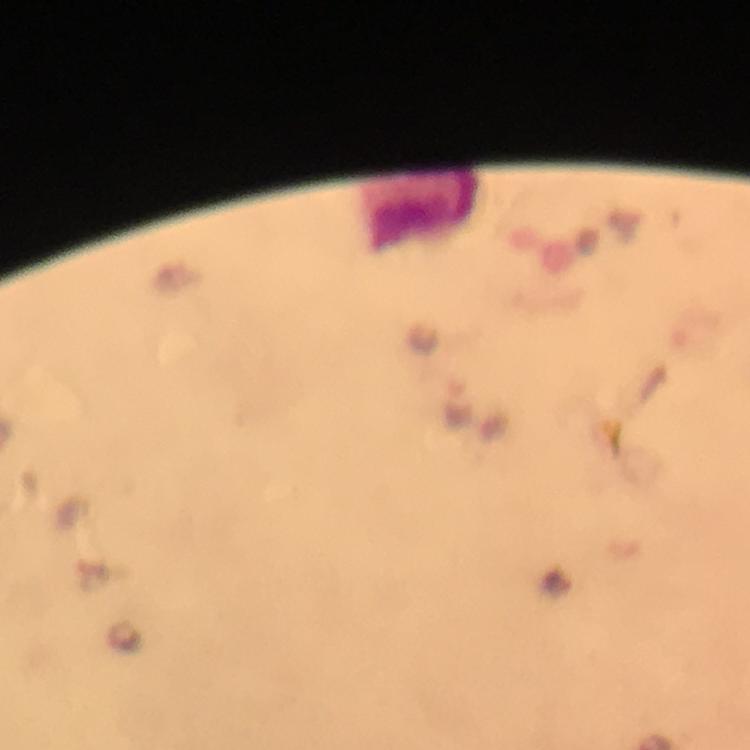

Approximate centers as (x, y) in pixels. Leukocyte locations: (418, 212). A crop from one field of view. Giemsa-stained preparation. Plasmodium parasites: none seen. From a diagnostic examination for malaria. Thick blood film. Image is 750×750 pixels. At 100x magnification. Immersion oil was used. Photographed with a smartphone mounted on the microscope.